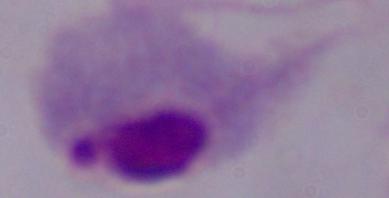

Summary:
  - Magnification: 1000x
  - Modality: micrograph
  - Identification: trichomonad